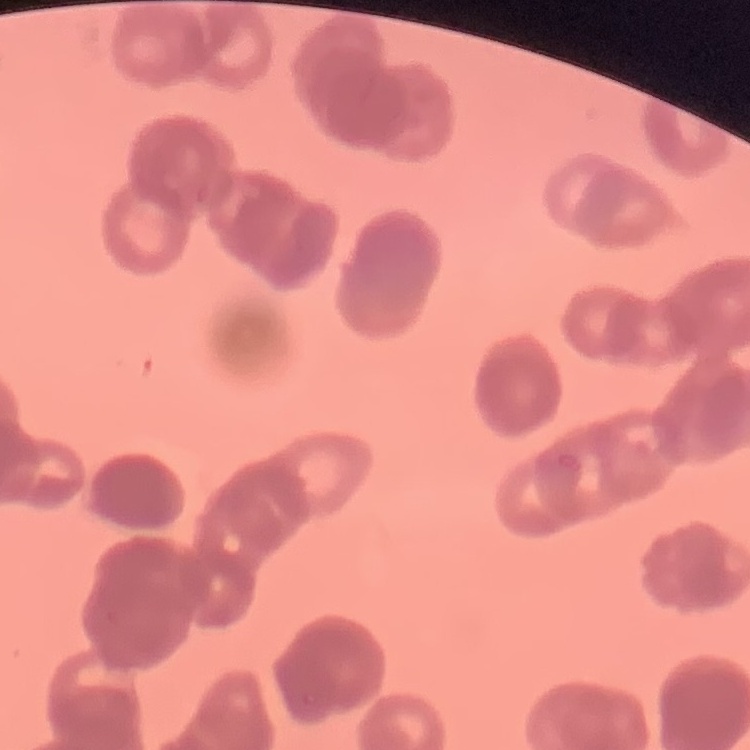
{
  "red_blood_cell_morphology": "rouleaux formation",
  "stain": "Field's or Giemsa",
  "preparation": "thin peripheral smear",
  "image_type": "one tile cut from a larger photomicrograph"
}